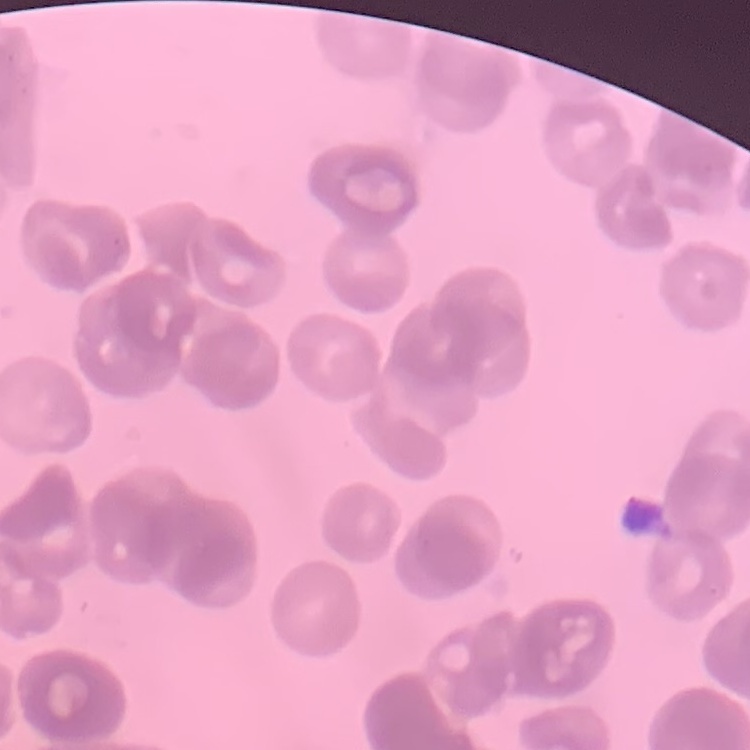
The red blood cells exhibit rouleaux formation. Square crop of a larger photomicrograph. Thin blood smear. Field's or Giemsa stain.